Locate every blood parasite and identify its species.
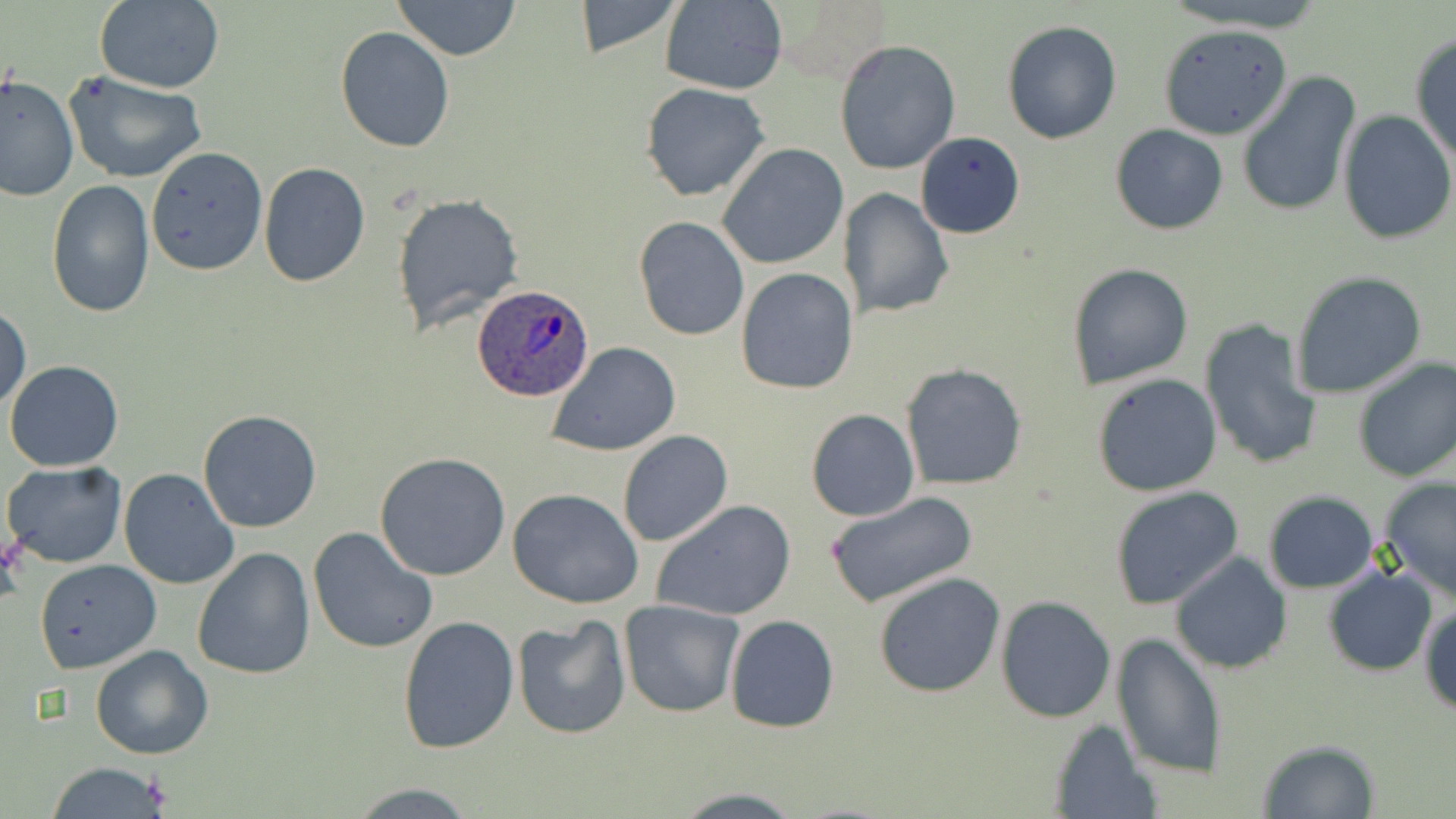

Approximate bounding boxes as [x1, y1, x2, y2] in pixels.
Plasmodium ovale-infected red blood cells: [472, 286, 594, 401].
No Plasmodium falciparum, Plasmodium malariae, Plasmodium vivax, Babesia divergens, or Trypanosoma brucei observed.

Summary:
  - Uninfected red blood cell locations: [95, 0, 224, 94], [390, 0, 524, 60], [658, 0, 786, 95], [1160, 0, 1334, 33], [571, 1, 686, 59], [1001, 18, 1123, 144], [1157, 25, 1296, 141], [335, 28, 455, 153], [1409, 33, 1456, 168], [833, 39, 963, 176], [63, 72, 209, 184], [1237, 72, 1360, 216], [0, 74, 79, 204], [640, 83, 770, 201], [1337, 110, 1454, 246], [1110, 124, 1228, 235], [915, 131, 1025, 240], [718, 144, 848, 270], [144, 147, 267, 276], [259, 164, 370, 286], [45, 180, 156, 320], [838, 187, 955, 320], [391, 192, 526, 335], [633, 217, 750, 342], [1066, 262, 1195, 391], [735, 268, 858, 396], [1290, 270, 1427, 399], [1, 303, 31, 414], [1198, 318, 1322, 472], [547, 343, 679, 457], [1351, 356, 1456, 484], [5, 359, 125, 472], [901, 362, 1027, 491], [1091, 373, 1223, 497], [806, 408, 920, 522], [197, 410, 324, 533], [618, 430, 733, 547], [375, 452, 511, 581], [2, 460, 127, 568], [117, 468, 239, 590], [1378, 477, 1456, 603], [1110, 487, 1244, 611], [508, 488, 644, 609], [1264, 490, 1380, 592], [824, 491, 978, 610], [650, 499, 799, 623], [308, 526, 439, 655], [192, 546, 315, 680], [1170, 553, 1292, 675], [33, 559, 161, 672], [1321, 565, 1438, 676], [873, 571, 1006, 698], [995, 595, 1117, 723], [618, 599, 745, 717], [1421, 603, 1455, 715], [724, 614, 841, 734], [397, 616, 519, 754], [512, 616, 631, 740], [1111, 632, 1227, 780], [90, 645, 214, 761], [1047, 718, 1162, 819], [1256, 739, 1381, 818], [45, 762, 172, 819], [344, 782, 483, 816]
  - Slide-level diagnosis: Plasmodium ovale
  - Stain: May-Grünwald-Giemsa
  - Modality: light microscopy
  - Field of view: one of a larger specimen
  - Magnification: 1000x
  - Preparation: thin blood smear
  - Image size: 1456×819 pixels